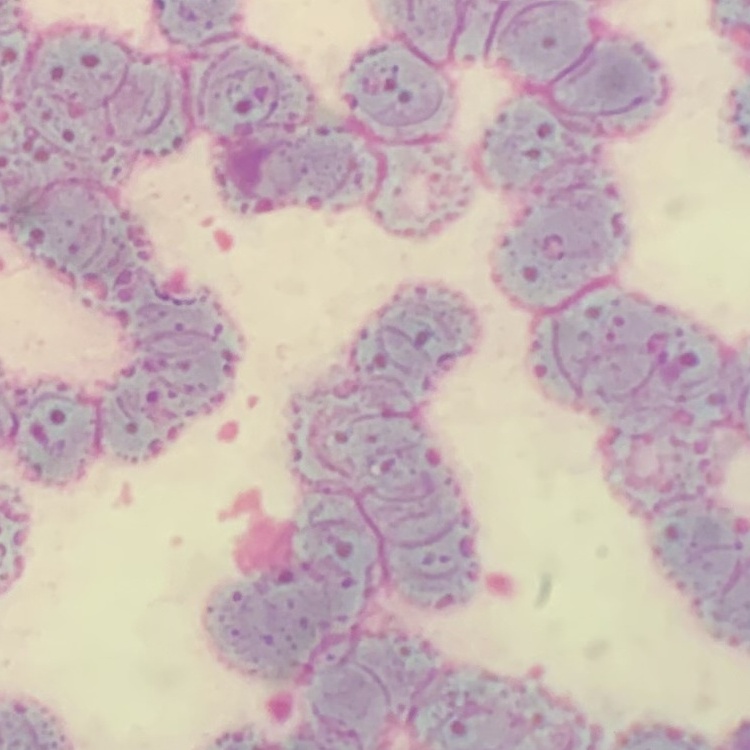
red blood cell morphology = rouleaux formation
image type = square crop of a larger photomicrograph
preparation = thin blood film
stain = Field's or Giemsa